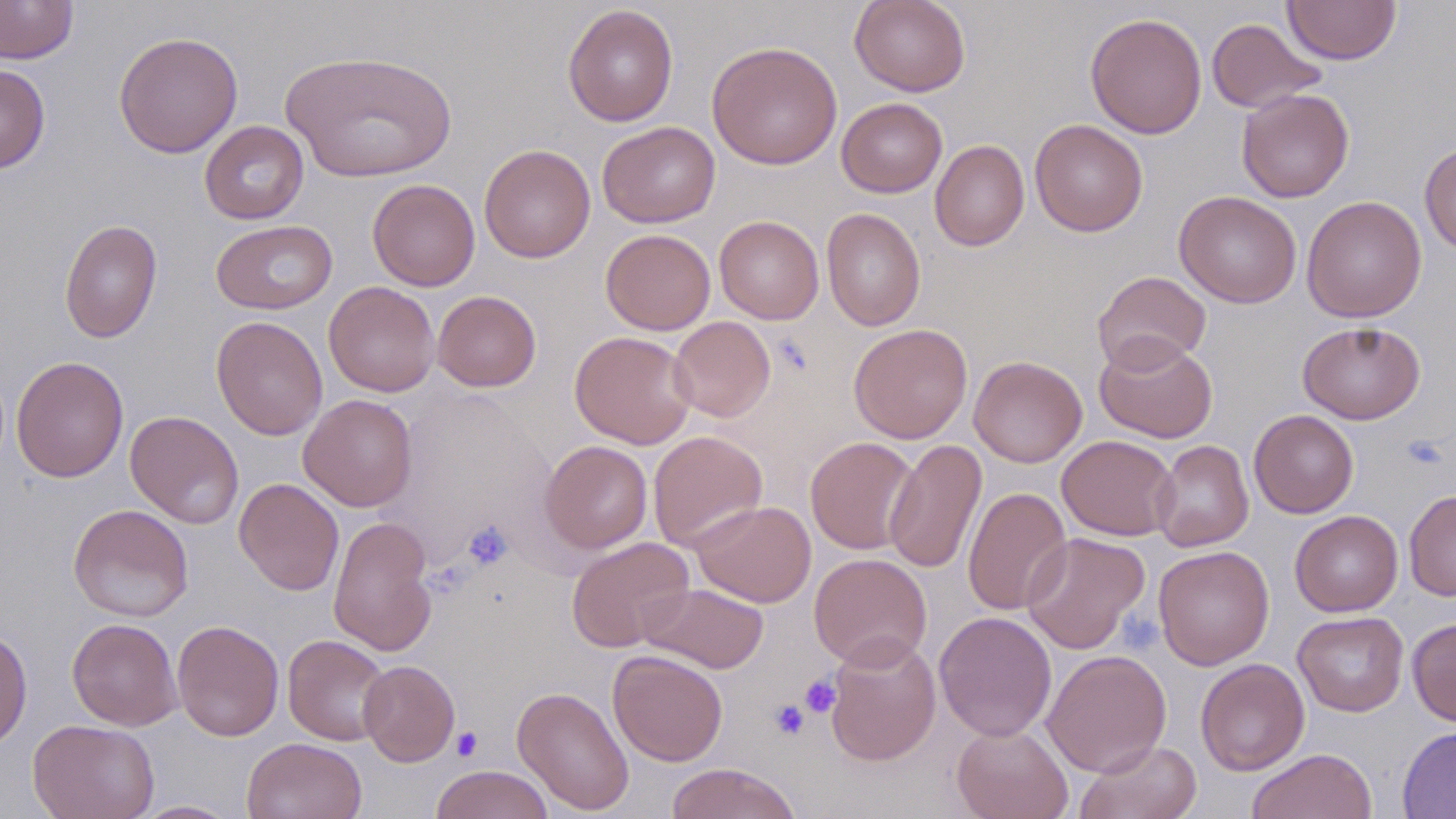

Approximate bounding boxes as (x1,y1)-(x2,y2) corner pairs in pixels. Uninfected red blood cell locations: (0,0)-(78,64), (849,0)-(971,97), (1283,0)-(1401,65), (563,4)-(679,127), (1085,12)-(1207,139), (1206,18)-(1327,114), (113,31)-(244,158), (706,41)-(843,170), (280,49)-(458,184), (0,63)-(51,174), (1236,87)-(1355,202), (836,98)-(947,198), (1030,119)-(1147,237), (199,120)-(309,224), (597,121)-(720,228), (930,139)-(1029,251), (479,143)-(595,263), (1419,143)-(1456,253), (367,178)-(480,291), (1173,191)-(1302,308), (1301,195)-(1427,323), (822,208)-(925,332), (714,215)-(824,324), (58,219)-(163,343), (211,219)-(337,315), (601,229)-(716,335), (1092,270)-(1212,373), (323,281)-(440,397), (433,290)-(541,392), (210,315)-(328,440), (668,316)-(776,422), (1297,321)-(1425,424), (848,323)-(973,443), (569,331)-(698,449), (1094,334)-(1218,444), (11,355)-(129,483), (968,355)-(1087,468), (298,394)-(418,512), (125,410)-(244,529), (1249,410)-(1359,518), (648,431)-(768,553), (1057,435)-(1179,541), (806,436)-(919,554), (883,439)-(986,575), (539,440)-(653,554), (1151,440)-(1253,552), (234,478)-(344,596), (962,486)-(1072,615), (1404,490)-(1456,601), (691,500)-(816,607), (68,504)-(194,622), (1290,510)-(1403,617), (328,515)-(437,657), (1021,532)-(1150,654), (567,536)-(695,652), (1153,545)-(1275,670), (809,552)-(932,670), (638,582)-(769,673), (934,611)-(1058,742), (1293,611)-(1409,717), (67,618)-(183,730), (1406,618)-(1456,726), (171,619)-(284,741), (0,625)-(33,751), (825,633)-(941,766), (282,634)-(392,746), (607,649)-(728,767), (1041,649)-(1172,777), (1195,658)-(1310,776), (358,660)-(459,766), (512,685)-(635,815), (28,718)-(159,819), (951,723)-(1073,819), (1397,725)-(1456,818), (242,737)-(367,819), (1075,739)-(1202,819), (1246,749)-(1377,819), (665,762)-(803,819), (431,765)-(554,819), (132,800)-(241,818). Platelet locations: (1402,435)-(1448,470), (463,520)-(514,571), (799,674)-(842,717), (769,698)-(810,740), (450,727)-(483,762). Slide-level diagnosis: no evidence of blood parasites. Image is 1456×819 pixels. Optical microscopy. One field of a larger specimen. 1000x magnification. May-Grünwald-Giemsa stain. Thin blood smear.